Assess this cell for malaria.
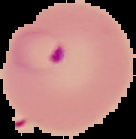
Parasitized.

Image is 136×139 pixels. From a thin blood smear. The area outside the segmented cell region is set to black.